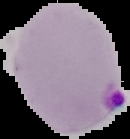

Image is 130×139 pixels. Malaria status: parasitized. The area outside the segmented cell region is set to black. From a thin blood smear.